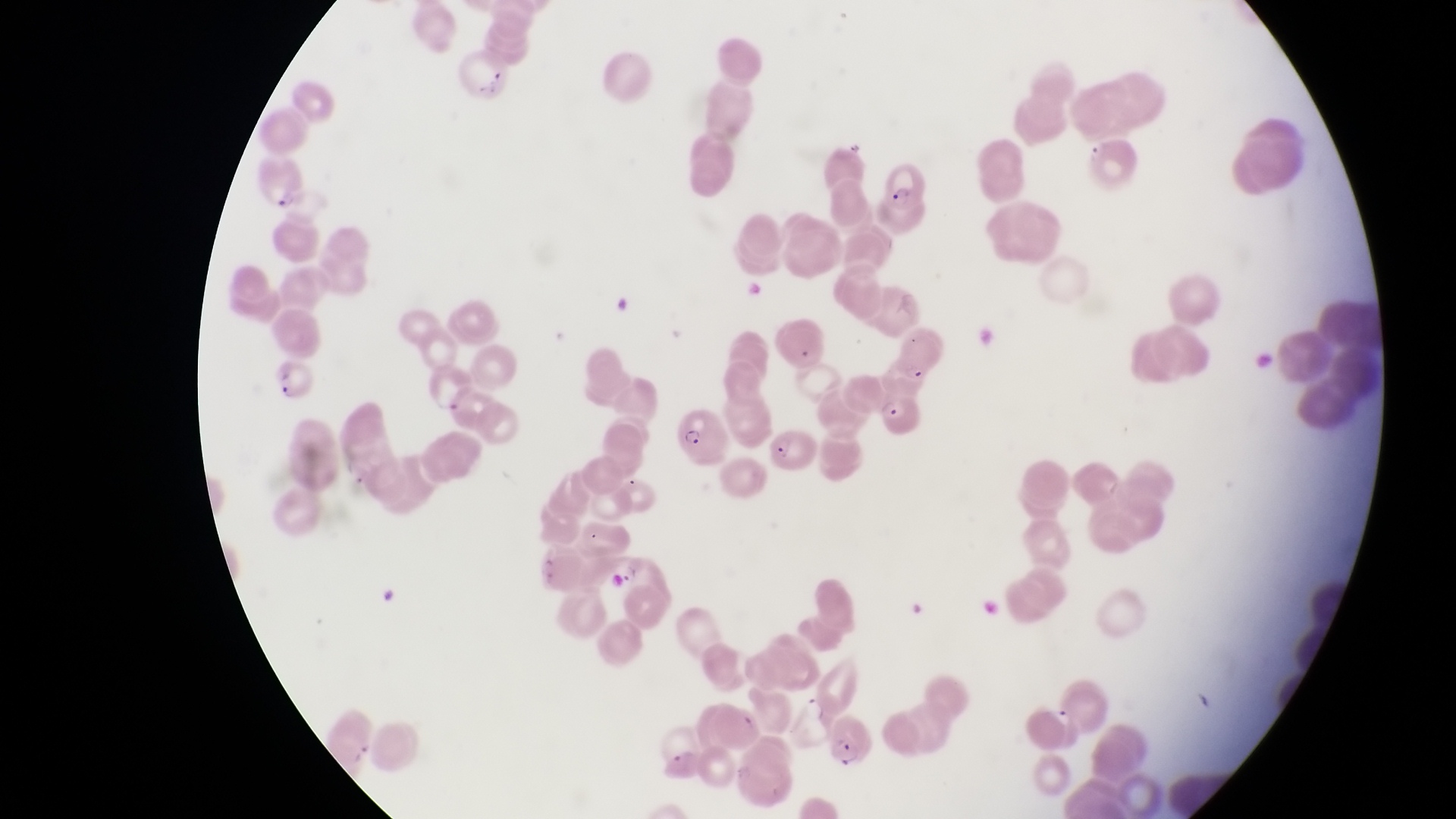 Approximate bounding boxes as {left, top, right, bottom} in pixels. Parasitised red blood cell locations: {258, 159, 316, 211}, {880, 159, 930, 215}, {274, 362, 317, 404}, {877, 386, 929, 444}, {679, 407, 734, 471}, {763, 422, 822, 481}, {616, 554, 677, 620}, {832, 714, 878, 772}. Artifact (platelet-like body, stain precipitate, or debris) locations: {457, 53, 517, 103}. Single field of view. Captured by a smartphone held over the eyepiece of an Olympus CX-23 microscope. Collected in Uganda. Image is 1456×819 pixels. Thin blood smear. Magnification of 1000x.